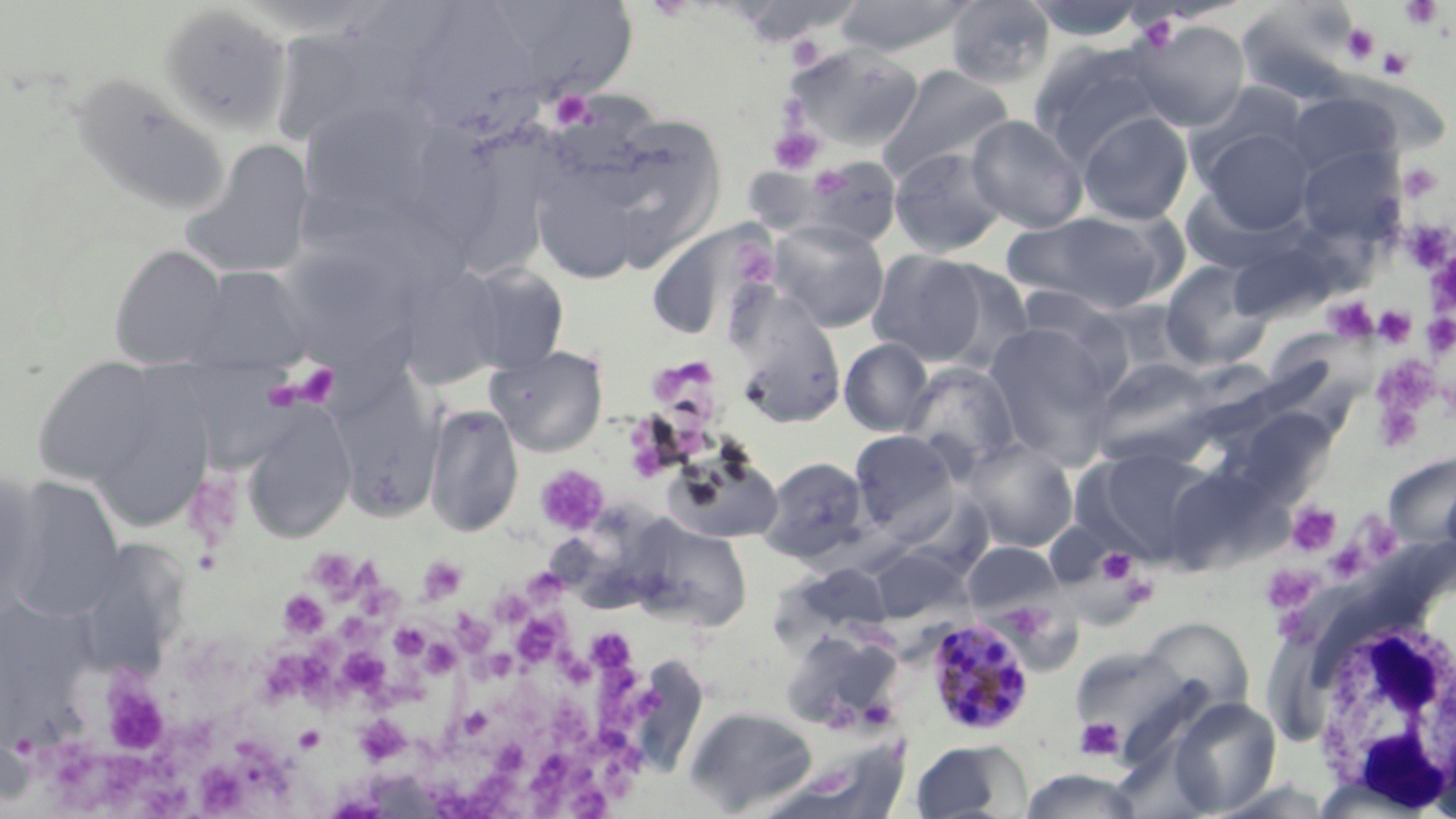 Approximate bounding boxes as (x1, y1, x2, y2) in pixels. Platelet locations: (1399, 0, 1445, 30), (1136, 12, 1181, 50), (1341, 22, 1381, 64), (786, 36, 825, 71), (1376, 47, 1414, 80), (549, 90, 595, 130), (767, 126, 824, 174), (1398, 162, 1443, 203), (1409, 231, 1448, 269), (744, 253, 775, 285), (1426, 263, 1455, 314), (1325, 297, 1376, 341), (1373, 305, 1417, 348), (1424, 309, 1455, 356), (677, 357, 711, 385), (1375, 357, 1441, 414), (278, 364, 340, 409), (652, 364, 688, 397), (1375, 408, 1426, 452), (534, 465, 609, 535), (196, 478, 247, 554), (1287, 501, 1341, 556), (1350, 505, 1398, 560), (1324, 542, 1369, 583), (1096, 548, 1140, 587), (320, 553, 366, 599), (418, 557, 467, 603), (1260, 565, 1316, 612), (530, 568, 562, 596), (366, 580, 403, 611), (279, 590, 330, 640), (491, 593, 527, 620), (1275, 608, 1310, 639), (454, 612, 491, 652), (517, 612, 567, 664), (336, 613, 381, 643), (388, 622, 431, 659), (597, 633, 634, 663), (428, 639, 465, 675), (485, 648, 520, 679), (560, 648, 598, 690), (340, 651, 389, 696), (264, 655, 335, 707), (597, 662, 658, 723), (377, 668, 432, 718), (97, 671, 171, 756), (461, 700, 489, 738), (559, 700, 594, 754), (357, 714, 409, 763), (170, 715, 224, 765), (1075, 716, 1125, 762), (595, 720, 642, 757), (497, 738, 527, 770), (46, 745, 98, 793), (237, 745, 291, 801), (528, 746, 595, 804), (103, 751, 153, 805), (603, 759, 641, 806), (201, 765, 247, 813), (433, 767, 516, 817), (142, 776, 197, 817). Plasmodium malariae-infected red blood cell locations: (925, 616, 1036, 737). White blood cell locations: (1309, 601, 1456, 807). Uninfected red blood cell locations: (831, 0, 978, 57), (945, 0, 1056, 90), (1021, 0, 1154, 41), (1245, 0, 1369, 107), (725, 1, 863, 46), (158, 4, 294, 136), (523, 5, 637, 98), (425, 7, 544, 144), (1130, 18, 1251, 131), (281, 30, 366, 133), (1029, 40, 1171, 163), (786, 43, 923, 152), (877, 65, 1014, 182), (1327, 70, 1443, 157), (69, 76, 230, 218), (1286, 92, 1401, 185), (298, 100, 439, 223), (1077, 111, 1193, 225), (626, 112, 728, 261), (966, 114, 1088, 233), (1196, 125, 1315, 235), (417, 135, 505, 254), (181, 140, 315, 280), (1295, 145, 1405, 248), (889, 147, 1008, 257), (800, 156, 902, 250), (534, 163, 637, 279), (1004, 210, 1177, 313), (769, 219, 890, 332), (654, 222, 774, 329), (109, 244, 229, 369), (868, 249, 988, 365), (1160, 258, 1275, 370), (926, 260, 1035, 372), (391, 261, 510, 390), (457, 262, 570, 375), (184, 265, 312, 373), (1013, 285, 1118, 360), (735, 313, 847, 427), (982, 322, 1119, 463), (1276, 332, 1378, 416), (839, 338, 935, 437), (487, 345, 609, 456), (1088, 355, 1217, 463), (30, 356, 167, 487), (901, 362, 1022, 475), (329, 375, 443, 520), (85, 389, 214, 532), (424, 403, 524, 537), (241, 408, 356, 545), (1249, 411, 1339, 494), (849, 429, 959, 533), (964, 439, 1078, 552), (1084, 445, 1219, 564), (664, 449, 783, 545), (760, 455, 870, 562), (1178, 458, 1310, 572), (1384, 462, 1455, 548), (0, 472, 40, 613), (3, 476, 126, 622), (632, 521, 753, 631), (963, 542, 1061, 615), (971, 545, 1086, 678), (870, 547, 962, 623), (92, 550, 168, 691), (1137, 616, 1254, 717), (780, 628, 904, 732), (1070, 645, 1196, 754), (1168, 697, 1281, 816), (685, 706, 818, 815), (1428, 721, 1456, 818), (910, 739, 1029, 818), (782, 741, 908, 819), (1020, 768, 1142, 819). Slide-level diagnosis: Plasmodium malariae. May-Grünwald-Giemsa-stained preparation. 1000x magnification. Optical microscopy. One field of a larger specimen. Image is 1456×819 pixels. Thin blood film.